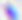
Captured at 400x magnification. Toxoplasma gondii is seen. Micrograph.